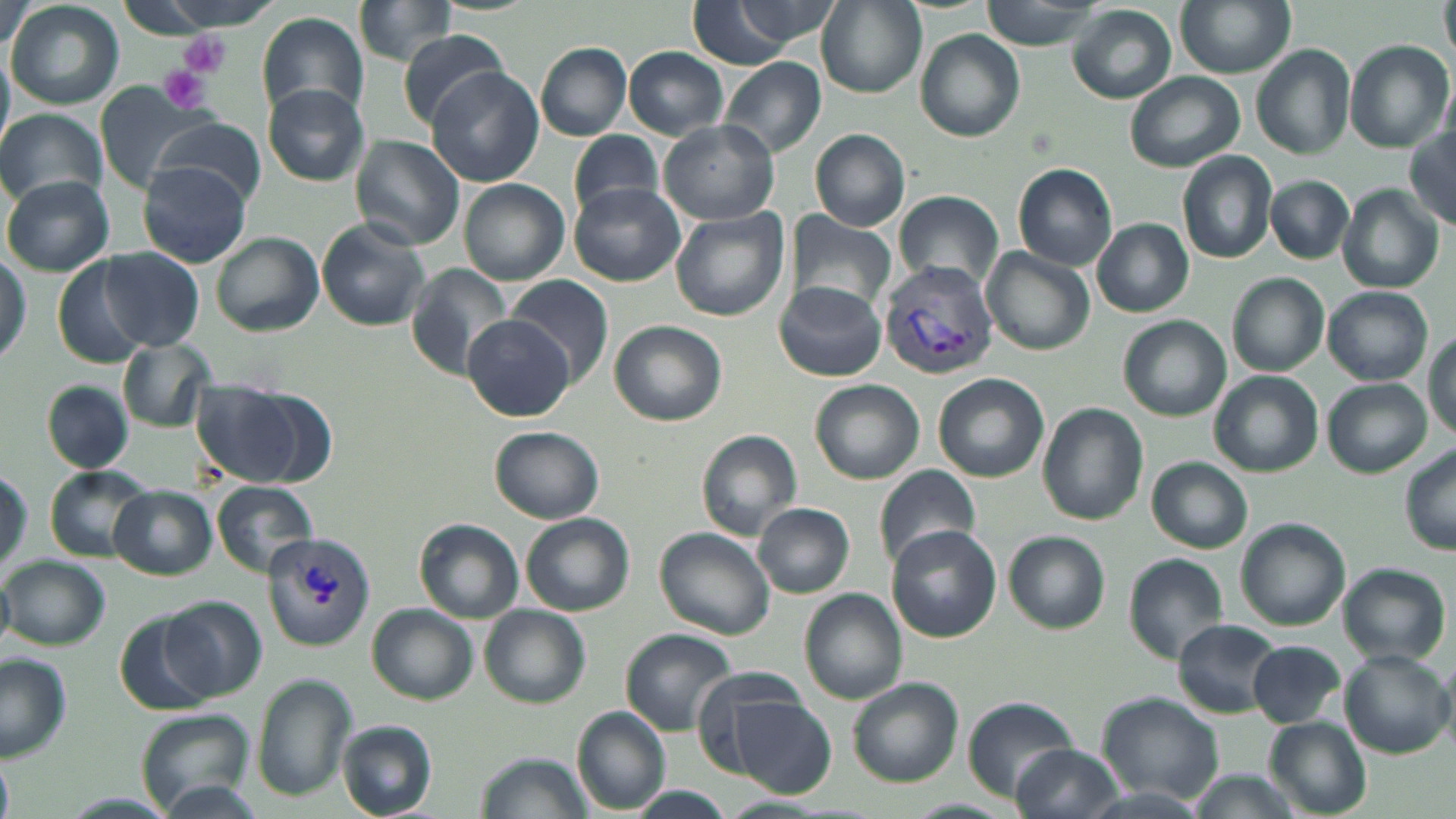

Summary:
  - Coordinate format: approximate bounding boxes as (x1, y1, x2, y2) in pixels
  - Platelet locations: (177, 30, 230, 79), (160, 66, 207, 114)
  - Plasmodium vivax-infected red blood cell locations: (876, 259, 999, 380), (261, 530, 376, 652)
  - Uninfected red blood cell locations: (160, 0, 274, 29), (684, 0, 817, 68), (720, 0, 846, 47), (978, 0, 1100, 51), (1174, 0, 1293, 77), (1441, 0, 1456, 66), (7, 1, 125, 109), (354, 1, 461, 68), (817, 2, 927, 98), (1068, 5, 1177, 104), (257, 10, 370, 124), (396, 29, 509, 129), (916, 29, 1025, 142), (1346, 40, 1451, 151), (535, 42, 633, 141), (1252, 45, 1355, 161), (624, 47, 728, 137), (0, 50, 13, 156), (718, 56, 828, 158), (426, 67, 543, 187), (1126, 72, 1244, 172), (261, 84, 369, 185), (92, 85, 223, 190), (0, 110, 106, 205), (146, 117, 267, 208), (659, 120, 779, 223), (1406, 124, 1456, 227), (810, 129, 910, 231), (571, 131, 666, 220), (349, 134, 465, 250), (1178, 150, 1278, 265), (136, 160, 254, 268), (1013, 163, 1117, 269), (1265, 174, 1354, 263), (4, 177, 114, 278), (459, 179, 570, 286), (568, 183, 685, 286), (1337, 184, 1443, 292), (895, 190, 1003, 288), (670, 208, 790, 323), (785, 211, 898, 317), (1092, 218, 1193, 316), (314, 219, 431, 331), (211, 232, 324, 336), (982, 248, 1095, 357), (99, 249, 205, 351), (0, 251, 29, 368), (49, 256, 159, 371), (405, 262, 515, 377), (1228, 273, 1329, 376), (508, 274, 614, 389), (773, 281, 887, 381), (1321, 287, 1433, 385), (465, 316, 573, 421), (1118, 316, 1231, 422), (608, 320, 726, 426), (1426, 331, 1456, 438), (117, 336, 217, 433), (1209, 371, 1322, 476), (935, 372, 1050, 484), (190, 379, 312, 488), (1324, 379, 1432, 475), (810, 380, 924, 486), (43, 381, 134, 473), (1037, 403, 1150, 524), (489, 426, 604, 524), (696, 429, 803, 540), (506, 430, 616, 610), (1399, 444, 1456, 555), (1148, 456, 1253, 554), (875, 464, 981, 571), (45, 466, 153, 563), (0, 469, 30, 576), (210, 480, 320, 578), (110, 486, 216, 579), (754, 503, 855, 598), (521, 513, 635, 615), (1235, 517, 1350, 631), (416, 518, 524, 622), (886, 524, 1001, 642), (654, 527, 776, 640), (1004, 531, 1110, 634), (1124, 553, 1229, 663), (4, 556, 109, 651), (1339, 564, 1450, 666), (800, 590, 907, 703), (159, 596, 266, 702), (369, 604, 479, 702), (480, 605, 590, 707), (117, 613, 221, 717), (1173, 620, 1280, 718), (620, 629, 735, 733), (1248, 640, 1344, 728), (1341, 650, 1451, 758), (0, 656, 72, 761), (688, 665, 812, 774), (254, 674, 357, 805), (845, 678, 962, 786), (1096, 693, 1223, 803), (724, 695, 837, 796), (963, 697, 1078, 799), (572, 707, 670, 813), (133, 708, 255, 814), (1267, 719, 1371, 816), (336, 720, 438, 818), (1009, 743, 1124, 819), (476, 750, 593, 819), (0, 757, 13, 819), (1183, 771, 1304, 818), (157, 781, 266, 818), (1069, 784, 1217, 819), (629, 787, 731, 818), (62, 791, 177, 816)
  - Slide-level diagnosis: Plasmodium vivax
  - Stain: May-Grünwald-Giemsa
  - Field of view: one of a larger specimen
  - Modality: light microscopy
  - Image size: 1456×819 pixels
  - Magnification: 1000x
  - Preparation: thin blood smear